Locate every leukocyte (white blood cell).
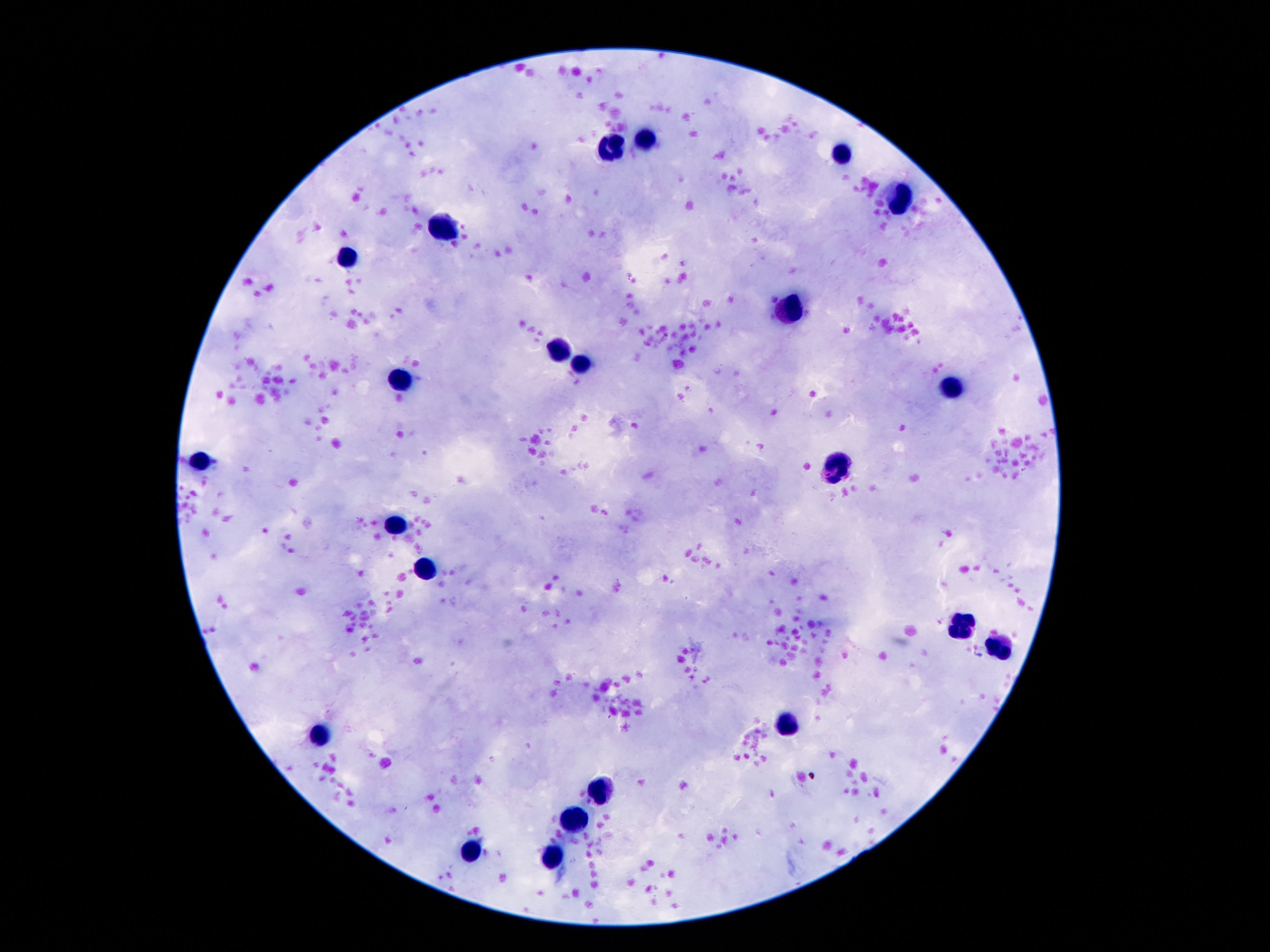
Approximate centers as [x, y] in pixels.
Leukocytes: [646, 138], [608, 148], [839, 155], [902, 198], [442, 226], [348, 260], [791, 309], [558, 350], [579, 361], [400, 380], [953, 388], [203, 461], [835, 471], [396, 521], [424, 567], [961, 627], [1001, 649], [791, 723], [319, 736], [600, 791], [573, 817], [472, 852], [552, 863].

field_of_view: single
image_size: 1270×952 pixels
stain: Giemsa
magnification: 100x
patient_malaria_status: negative
capture: smartphone camera through the microscope eyepiece
preparation: thick blood film